Give the position of every leukocyte visible.
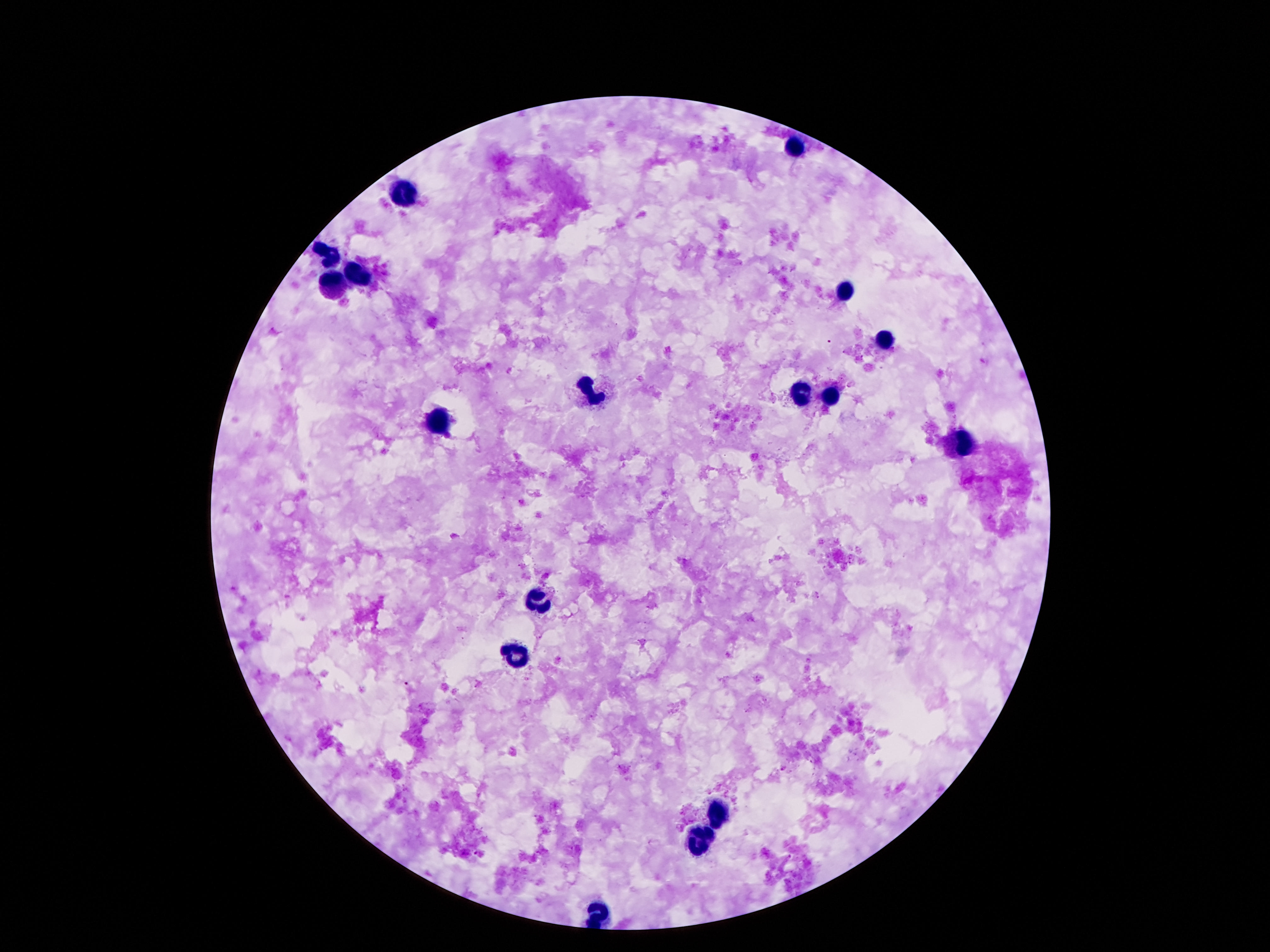

Approximate object centers, in pixels from the top-left corner.
Leukocytes: (x=793, y=151), (x=403, y=193), (x=330, y=258), (x=359, y=272), (x=337, y=290), (x=844, y=290), (x=886, y=343), (x=802, y=392), (x=592, y=395), (x=828, y=401), (x=435, y=425), (x=958, y=442), (x=545, y=604), (x=517, y=656), (x=718, y=810), (x=701, y=841), (x=599, y=916).

Thick blood smear. Giemsa-stained preparation. 100x magnification. Patient malaria status: not infected. Smartphone photograph taken through the microscope eyepiece. One field from this slide. Image is 1270×952 pixels.